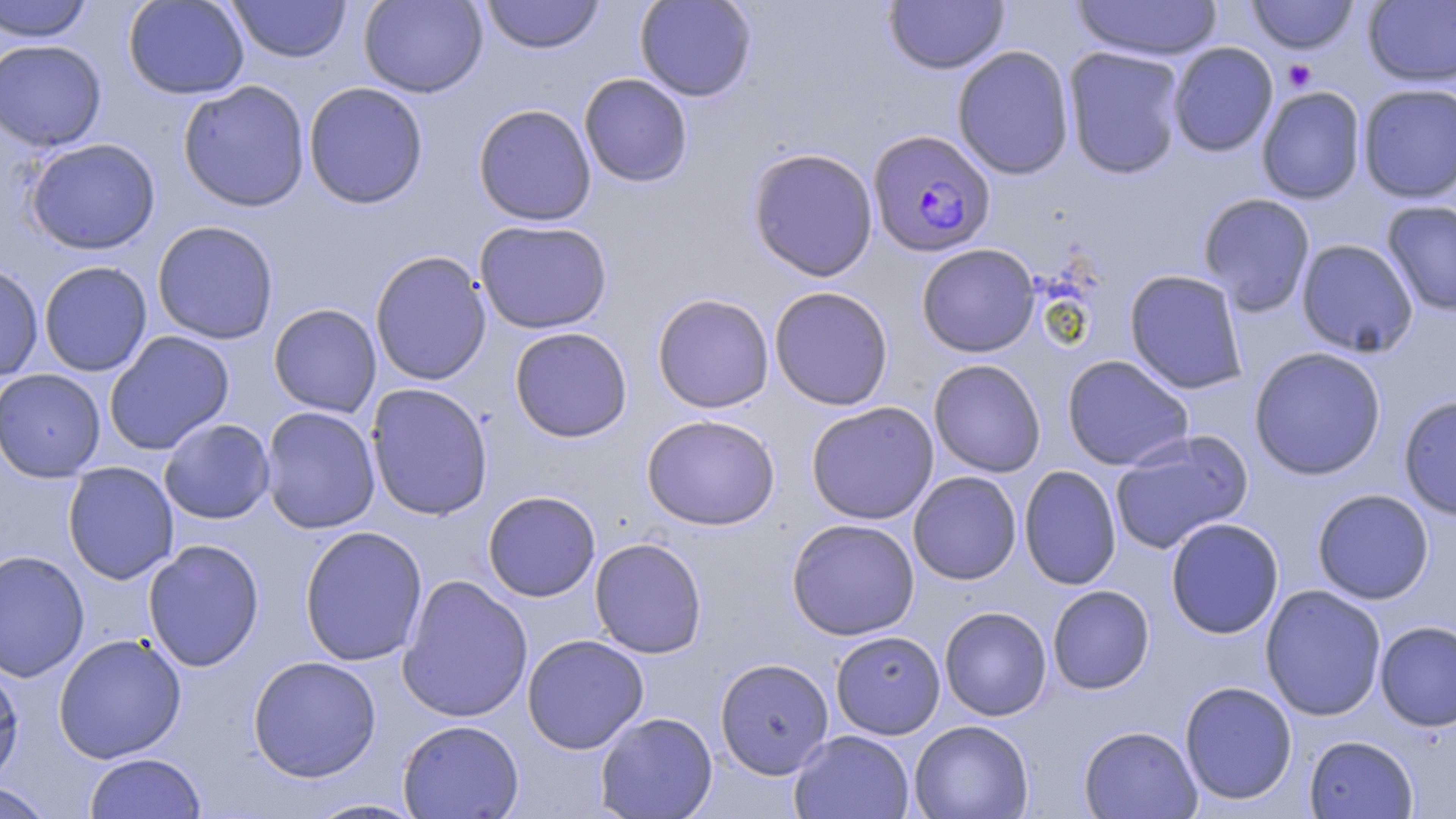

Summary:
  - Coordinate format: approximate bounding boxes as (x1,y1)-(x2,y2) corner pairs in pixels
  - Uninfected red blood cell locations: (0,0)-(94,42), (122,0)-(250,100), (358,0)-(488,98), (480,0)-(605,54), (634,0)-(757,102), (1071,0)-(1222,61), (1246,0)-(1359,54), (227,1)-(351,63), (883,1)-(1009,74), (1363,1)-(1456,87), (0,39)-(107,152), (1168,42)-(1278,157), (952,45)-(1075,180), (1063,46)-(1187,179), (579,73)-(693,187), (177,80)-(311,212), (303,82)-(429,209), (1357,84)-(1456,203), (1256,86)-(1367,204), (472,104)-(597,226), (24,138)-(160,255), (747,147)-(879,282), (1198,193)-(1316,316), (1381,200)-(1456,316), (474,219)-(612,334), (152,220)-(279,344), (1296,238)-(1418,358), (916,243)-(1040,357), (370,251)-(492,386), (38,261)-(152,377), (0,262)-(44,381), (1124,269)-(1249,395), (769,286)-(894,411), (651,293)-(775,413), (268,303)-(382,418), (509,326)-(633,442), (104,330)-(235,455), (1248,346)-(1387,481), (1061,355)-(1194,471), (928,359)-(1046,477), (926,361)-(1187,474), (0,369)-(106,482), (366,382)-(493,521), (1398,394)-(1456,520), (805,401)-(939,524), (260,406)-(381,534), (641,413)-(780,531), (158,418)-(275,524), (1109,430)-(1253,554), (63,461)-(179,584), (1019,465)-(1122,590), (908,471)-(1022,585), (1312,488)-(1434,604), (483,490)-(601,602), (1165,517)-(1284,639), (786,518)-(920,640), (299,525)-(428,667), (589,537)-(708,658), (143,539)-(265,672), (0,549)-(90,683), (397,574)-(533,723), (1260,584)-(1387,721), (1047,585)-(1155,694), (939,606)-(1053,721), (1374,620)-(1456,731), (830,630)-(946,739), (53,632)-(187,763), (522,634)-(649,754), (247,655)-(382,782), (0,657)-(24,789), (715,658)-(835,778), (1179,680)-(1297,805), (594,711)-(718,818), (397,719)-(524,818), (909,719)-(1034,819), (1078,725)-(1202,818), (789,730)-(914,819), (1303,735)-(1418,818), (84,752)-(206,818), (0,781)-(56,819), (305,798)-(428,818)
  - Platelet locations: (1282,59)-(1317,91)
  - Plasmodium falciparum-infected red blood cell locations: (868,129)-(996,258)
  - Slide-level diagnosis: Plasmodium falciparum
  - Field of view: single
  - Image size: 1456×819 pixels
  - Magnification: 1000x
  - Preparation: thin blood smear
  - Modality: light microscopy
  - Stain: May-Grünwald-Giemsa